Report the malaria status of this cell.
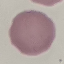
Uninfected.

{
  "image_type": "automatically extracted cell patch, resized to 64 × 64 pixels",
  "stain": "Giemsa",
  "capture": "smartphone through the microscope eyepiece",
  "preparation": "thin smear"
}